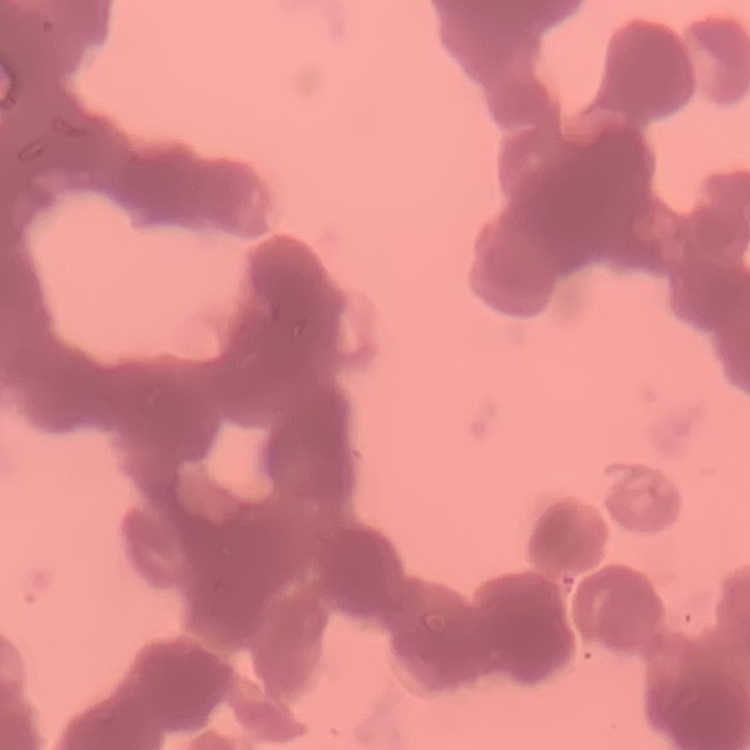

erythrocyte morphology = rouleaux formation
image type = square crop of a larger photomicrograph
preparation = thin blood smear
stain = Field's or Giemsa